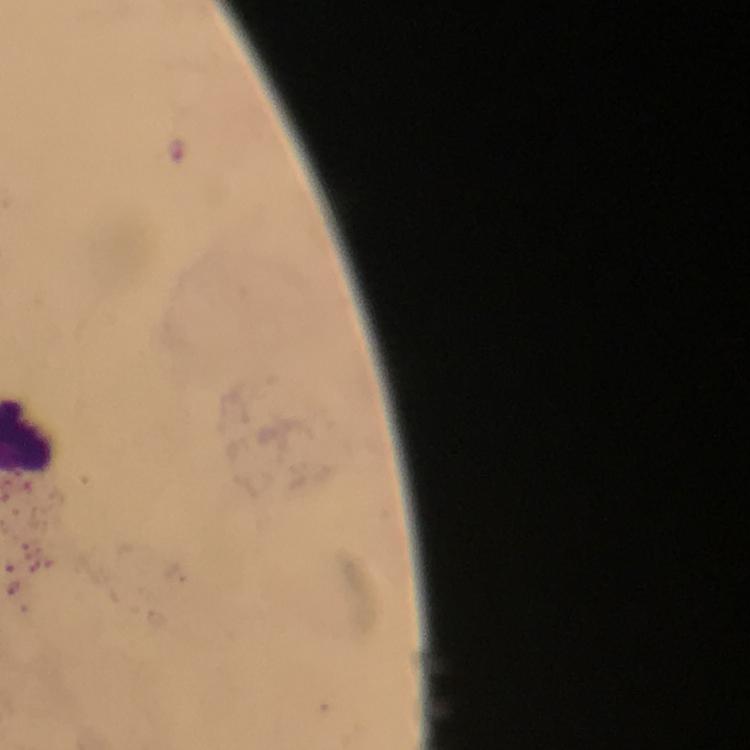

Approximate centers as (x, y) in pixels. Plasmodium parasite locations: (177, 148). From a diagnostic examination for malaria. Immersion oil was used. Giemsa stain. 100x magnification. Cropped region of a single field of view. Thick blood film. Image is 750×750 pixels. Smartphone photograph taken through a microscope.